Assess this cell for malaria.
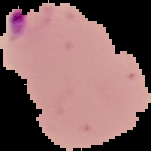

Parasitized.

preparation = thin blood smear
image size = 151×151 pixels
image type = segmented cell region with the area outside set to black